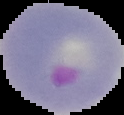
Summary:
  - Result: malaria parasites detected
  - Image size: 124×115 pixels
  - Image type: cell region segmented out of the field of view; surrounding area masked to black
  - Preparation: thin blood smear